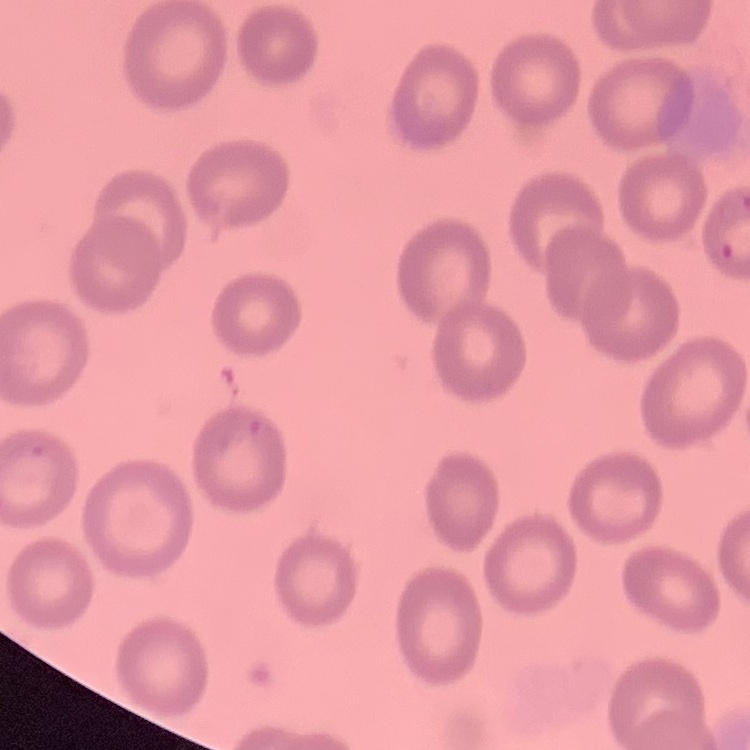

Summary:
  - Red blood cell morphology: no rouleaux formation
  - Stain: Field's or Giemsa
  - Image type: one tile cut from a larger photomicrograph
  - Preparation: thin blood smear